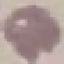
malaria status = uninfected
image type = automatically extracted cell patch, resized to 64 × 64 pixels
capture = smartphone through the microscope eyepiece
stain = Giemsa
preparation = thin smear